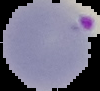

Summary:
  - Preparation: thin blood film
  - Malaria status: parasitized
  - Image size: 100×91 pixels
  - Image type: segmented cell region with the area outside set to black